Identify the parasite.
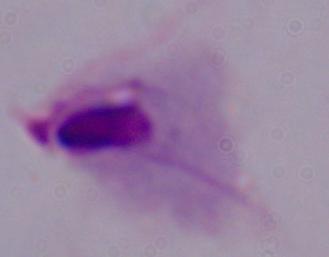
This is a trichomonad.

Summary:
  - Modality: micrograph
  - Magnification: 1000x